Report the malaria status of this cell.
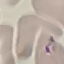

Parasitized.

Summary:
  - Capture: smartphone through the microscope eyepiece
  - Image type: automatically extracted cell patch, resized to 64 × 64 pixels
  - Preparation: thin blood film
  - Stain: Giemsa